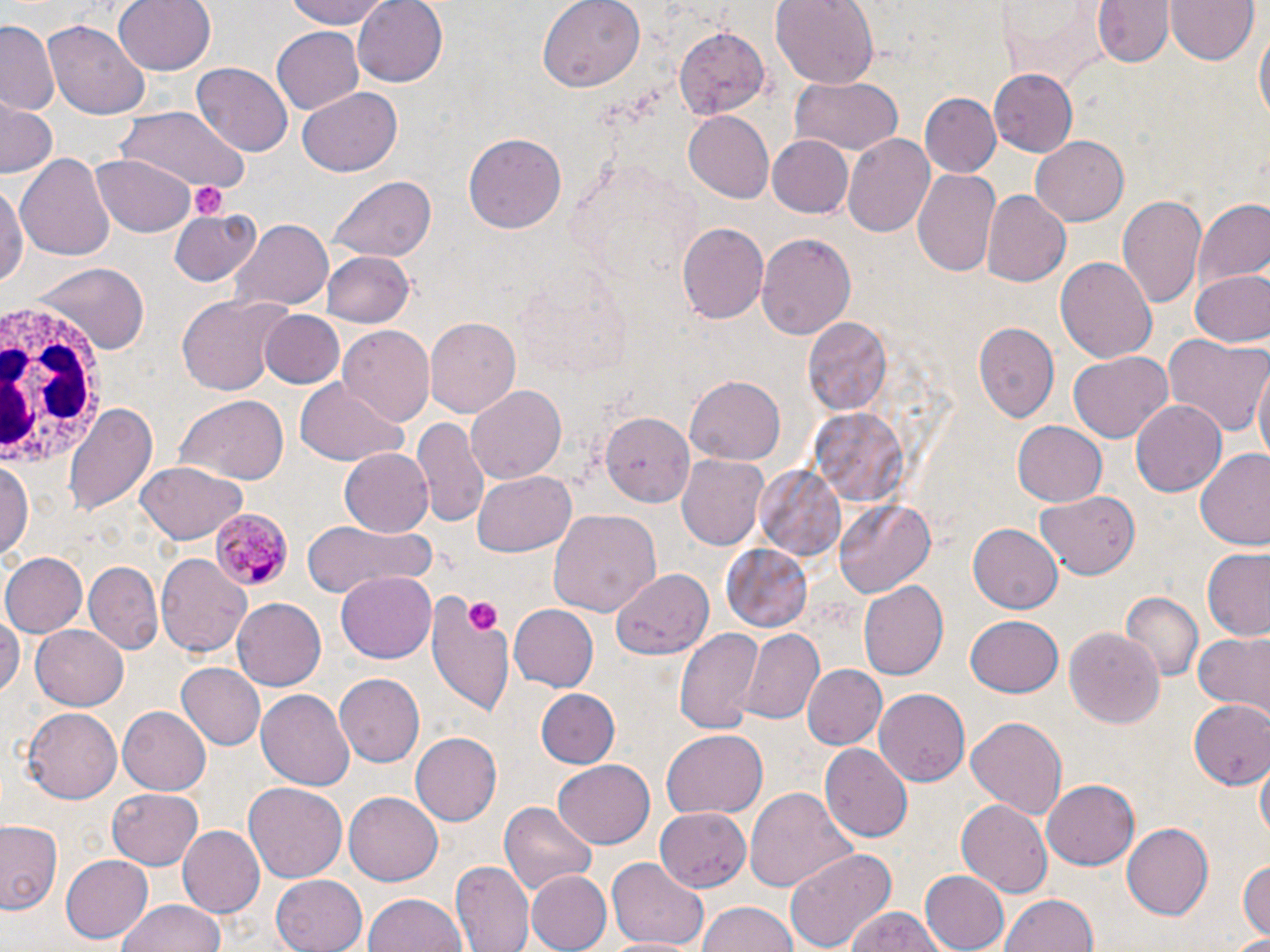
slide-level diagnosis = Plasmodium malariae
magnification = 1000x
white blood cell locations = approximate bounding boxes as named x1/y1/x2/y2 corners in pixels: (x1=1, y1=302, x2=102, y2=475)
field of view = single
image size = 1270×952 pixels
stain = May-Grünwald-Giemsa
platelet locations = approximate bounding boxes as named x1/y1/x2/y2 corners in pixels: (x1=192, y1=181, x2=228, y2=219), (x1=469, y1=599, x2=500, y2=630)
preparation = thin blood smear
Plasmodium malariae-infected red blood cell locations = approximate bounding boxes as named x1/y1/x2/y2 corners in pixels: (x1=208, y1=508, x2=291, y2=593)
modality = light microscopy
uninfected red blood cell locations = approximate bounding boxes as named x1/y1/x2/y2 corners in pixels: (x1=114, y1=0, x2=216, y2=76), (x1=281, y1=0, x2=399, y2=28), (x1=353, y1=0, x2=449, y2=87), (x1=539, y1=0, x2=646, y2=91), (x1=770, y1=0, x2=879, y2=90), (x1=1093, y1=0, x2=1174, y2=69), (x1=998, y1=1, x2=1106, y2=84), (x1=1167, y1=1, x2=1257, y2=66), (x1=1, y1=19, x2=60, y2=115), (x1=46, y1=19, x2=150, y2=119), (x1=1254, y1=25, x2=1269, y2=130), (x1=270, y1=26, x2=365, y2=116), (x1=675, y1=27, x2=769, y2=119), (x1=193, y1=64, x2=292, y2=157), (x1=989, y1=71, x2=1081, y2=156), (x1=915, y1=74, x2=1061, y2=166), (x1=789, y1=76, x2=904, y2=156), (x1=298, y1=87, x2=403, y2=176), (x1=918, y1=92, x2=1001, y2=178), (x1=0, y1=100, x2=57, y2=178), (x1=115, y1=108, x2=247, y2=191), (x1=683, y1=111, x2=775, y2=202), (x1=463, y1=131, x2=567, y2=233), (x1=842, y1=134, x2=937, y2=239), (x1=1029, y1=137, x2=1129, y2=226), (x1=767, y1=138, x2=852, y2=216), (x1=92, y1=153, x2=197, y2=236), (x1=17, y1=154, x2=114, y2=262), (x1=913, y1=167, x2=1002, y2=278), (x1=0, y1=176, x2=26, y2=293), (x1=327, y1=176, x2=436, y2=264), (x1=981, y1=190, x2=1070, y2=285), (x1=1117, y1=193, x2=1207, y2=309), (x1=1191, y1=198, x2=1269, y2=292), (x1=170, y1=207, x2=260, y2=287), (x1=231, y1=219, x2=333, y2=311), (x1=675, y1=222, x2=768, y2=324), (x1=756, y1=233, x2=856, y2=339), (x1=322, y1=251, x2=415, y2=328), (x1=1055, y1=256, x2=1158, y2=365), (x1=26, y1=260, x2=147, y2=355), (x1=1187, y1=270, x2=1269, y2=347), (x1=174, y1=294, x2=288, y2=398), (x1=262, y1=310, x2=344, y2=388), (x1=425, y1=317, x2=519, y2=419), (x1=802, y1=318, x2=893, y2=415), (x1=973, y1=322, x2=1058, y2=421), (x1=339, y1=326, x2=435, y2=428), (x1=1163, y1=333, x2=1270, y2=439), (x1=1067, y1=353, x2=1174, y2=441), (x1=1253, y1=367, x2=1269, y2=471), (x1=686, y1=375, x2=786, y2=466), (x1=293, y1=379, x2=408, y2=466), (x1=466, y1=385, x2=566, y2=484), (x1=171, y1=394, x2=289, y2=485), (x1=1131, y1=400, x2=1227, y2=497), (x1=63, y1=403, x2=156, y2=515), (x1=811, y1=407, x2=912, y2=510), (x1=598, y1=410, x2=695, y2=501), (x1=412, y1=416, x2=491, y2=532), (x1=1011, y1=420, x2=1106, y2=507), (x1=339, y1=448, x2=434, y2=537), (x1=1195, y1=449, x2=1270, y2=551), (x1=676, y1=454, x2=769, y2=553), (x1=1, y1=456, x2=34, y2=564), (x1=134, y1=462, x2=246, y2=544), (x1=754, y1=466, x2=847, y2=566), (x1=470, y1=470, x2=574, y2=556), (x1=1037, y1=490, x2=1139, y2=577), (x1=834, y1=499, x2=935, y2=600), (x1=549, y1=508, x2=661, y2=616), (x1=298, y1=519, x2=436, y2=599), (x1=967, y1=522, x2=1063, y2=614), (x1=721, y1=543, x2=814, y2=632), (x1=1202, y1=550, x2=1270, y2=640), (x1=0, y1=551, x2=87, y2=639), (x1=156, y1=554, x2=251, y2=657), (x1=84, y1=560, x2=163, y2=653), (x1=612, y1=568, x2=714, y2=662), (x1=336, y1=569, x2=436, y2=661), (x1=858, y1=579, x2=949, y2=682), (x1=423, y1=588, x2=517, y2=724), (x1=1120, y1=593, x2=1203, y2=684), (x1=231, y1=598, x2=326, y2=691), (x1=0, y1=603, x2=21, y2=705), (x1=508, y1=606, x2=598, y2=692), (x1=963, y1=616, x2=1064, y2=695), (x1=32, y1=624, x2=130, y2=711), (x1=1065, y1=626, x2=1164, y2=730), (x1=674, y1=628, x2=764, y2=735), (x1=739, y1=628, x2=824, y2=726), (x1=1192, y1=631, x2=1270, y2=716), (x1=176, y1=661, x2=268, y2=751), (x1=805, y1=664, x2=886, y2=750), (x1=334, y1=674, x2=424, y2=768), (x1=875, y1=687, x2=974, y2=784), (x1=258, y1=688, x2=355, y2=791), (x1=535, y1=689, x2=620, y2=769), (x1=1188, y1=699, x2=1270, y2=789), (x1=119, y1=705, x2=212, y2=793), (x1=21, y1=708, x2=120, y2=804), (x1=965, y1=714, x2=1068, y2=821), (x1=662, y1=731, x2=767, y2=817), (x1=409, y1=732, x2=500, y2=825), (x1=820, y1=743, x2=912, y2=842), (x1=551, y1=760, x2=656, y2=850), (x1=1256, y1=761, x2=1269, y2=847), (x1=1042, y1=778, x2=1140, y2=870), (x1=243, y1=781, x2=347, y2=884), (x1=745, y1=786, x2=858, y2=893), (x1=107, y1=789, x2=204, y2=869), (x1=343, y1=792, x2=441, y2=887), (x1=955, y1=798, x2=1053, y2=898), (x1=501, y1=800, x2=597, y2=900), (x1=655, y1=808, x2=750, y2=891), (x1=0, y1=819, x2=61, y2=915), (x1=1121, y1=824, x2=1213, y2=919), (x1=179, y1=827, x2=265, y2=915), (x1=784, y1=846, x2=899, y2=950), (x1=59, y1=854, x2=152, y2=943), (x1=607, y1=857, x2=708, y2=949), (x1=1238, y1=857, x2=1270, y2=940), (x1=451, y1=861, x2=532, y2=952), (x1=522, y1=869, x2=611, y2=952), (x1=919, y1=869, x2=1010, y2=951), (x1=272, y1=874, x2=367, y2=952), (x1=365, y1=893, x2=468, y2=952), (x1=1001, y1=893, x2=1100, y2=952), (x1=117, y1=900, x2=225, y2=952), (x1=694, y1=901, x2=800, y2=952), (x1=842, y1=908, x2=950, y2=952), (x1=1233, y1=932, x2=1270, y2=951), (x1=605, y1=935, x2=690, y2=952)